State the blood parasite species.
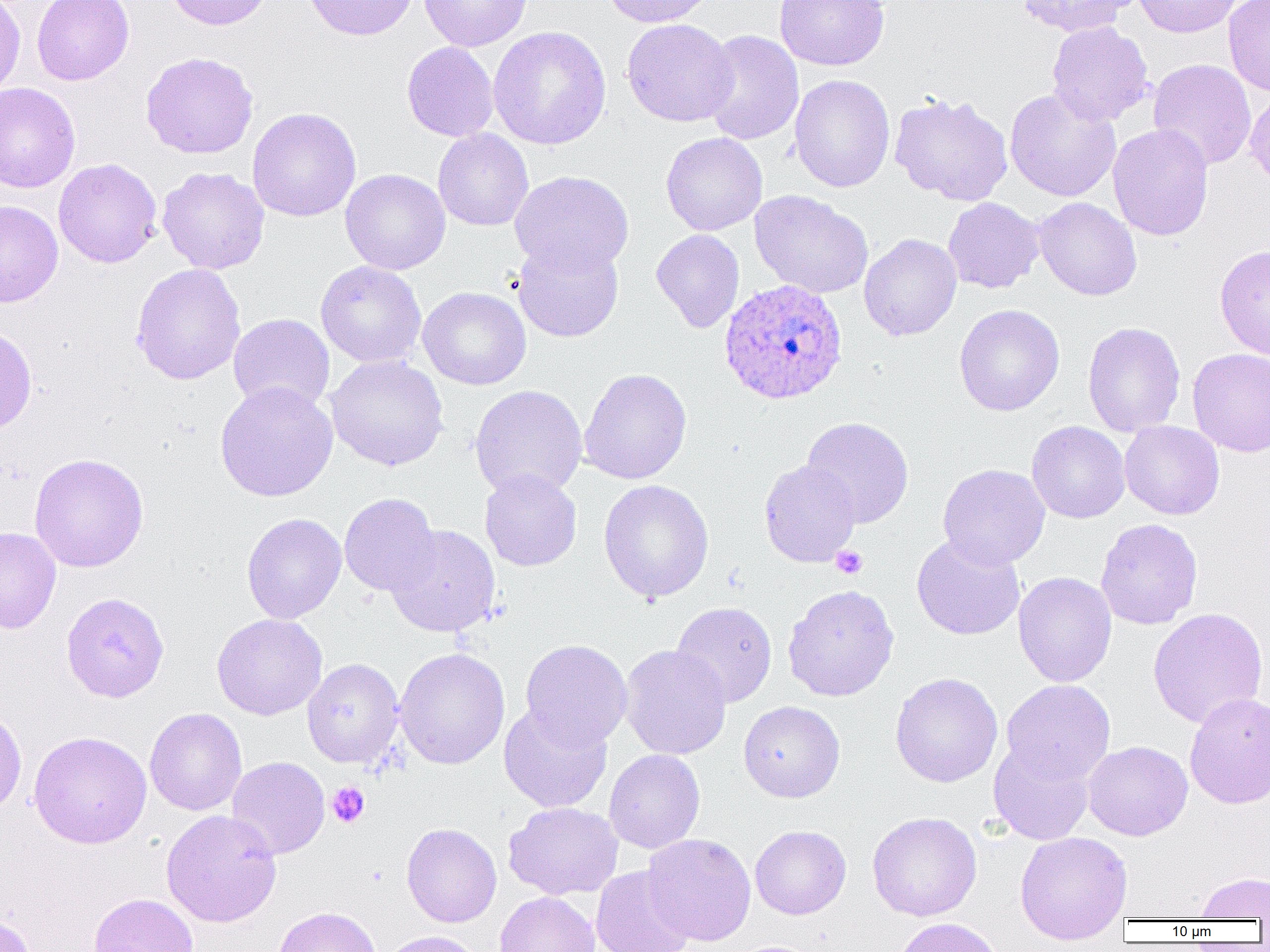

Plasmodium ovale.

uninfected red blood cell locations = approximate bounding boxes as [x1, y1, x2, y2] in pixels: [0, 0, 26, 99], [32, 0, 134, 85], [163, 0, 273, 30], [303, 0, 417, 41], [419, 0, 532, 51], [601, 0, 716, 27], [774, 0, 889, 70], [1016, 0, 1135, 37], [1133, 0, 1243, 38], [1223, 0, 1270, 96], [622, 19, 739, 127], [1046, 21, 1154, 126], [488, 26, 611, 150], [699, 30, 804, 146], [402, 42, 499, 142], [140, 51, 259, 159], [152, 53, 261, 276], [1147, 58, 1257, 170], [789, 74, 895, 193], [0, 83, 81, 192], [1244, 87, 1270, 189], [1005, 88, 1121, 202], [889, 92, 1014, 206], [247, 107, 362, 222], [1108, 123, 1214, 241], [433, 129, 534, 231], [661, 132, 767, 236], [53, 158, 162, 268], [157, 167, 269, 274], [341, 168, 450, 274], [510, 170, 633, 275], [750, 190, 874, 298], [942, 197, 1044, 293], [1034, 197, 1141, 301], [0, 200, 63, 307], [651, 229, 744, 333], [859, 233, 962, 341], [512, 240, 624, 342], [1215, 245, 1270, 361], [315, 261, 427, 368], [130, 263, 246, 385], [418, 286, 532, 390], [954, 304, 1065, 416], [228, 313, 335, 414], [1082, 321, 1186, 437], [0, 324, 37, 434], [1187, 347, 1270, 457], [326, 355, 448, 471], [579, 368, 692, 485], [214, 381, 338, 502], [470, 384, 587, 499], [801, 416, 914, 529], [1027, 420, 1130, 523], [1119, 421, 1224, 520], [28, 452, 149, 573], [759, 459, 861, 567], [937, 464, 1050, 570], [479, 469, 582, 572], [598, 479, 714, 603], [339, 492, 440, 597], [242, 504, 439, 605], [241, 512, 347, 624], [1095, 518, 1203, 629], [385, 524, 501, 637], [0, 526, 61, 634], [911, 534, 1026, 640], [1013, 571, 1117, 687], [782, 584, 899, 702], [60, 592, 169, 702], [670, 601, 777, 708], [1147, 607, 1268, 729], [211, 613, 327, 720], [520, 639, 633, 749], [619, 644, 731, 759], [394, 647, 510, 769], [302, 658, 405, 768], [890, 672, 1003, 787], [1001, 679, 1116, 785], [1184, 691, 1270, 809], [738, 700, 845, 802], [499, 702, 612, 813], [0, 707, 27, 817], [144, 708, 247, 816], [29, 730, 152, 849], [988, 739, 1095, 845], [1083, 740, 1193, 841], [604, 749, 705, 853], [226, 757, 330, 859], [504, 801, 623, 900], [160, 809, 282, 927], [867, 811, 982, 921], [401, 823, 502, 927], [750, 825, 851, 919], [1014, 831, 1133, 944], [641, 833, 756, 945], [590, 865, 695, 952], [1195, 872, 1270, 919], [494, 891, 599, 952], [88, 893, 199, 952], [272, 906, 381, 952], [0, 913, 36, 952], [893, 917, 1004, 952], [377, 930, 483, 952]
platelet locations = approximate bounding boxes as [x1, y1, x2, y2] in pixels: [830, 545, 868, 579], [327, 782, 370, 827]
preparation = thin blood film
Plasmodium ovale-infected red blood cell locations = approximate bounding boxes as [x1, y1, x2, y2] in pixels: [718, 279, 848, 406]
image size = 1270×952 pixels
modality = optical microscopy
field of view = single
magnification = 1000x